Assess this cell for malaria.
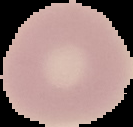

It is uninfected.

From a thin blood film. Segmented cell region on a black background. Image is 133×127 pixels.